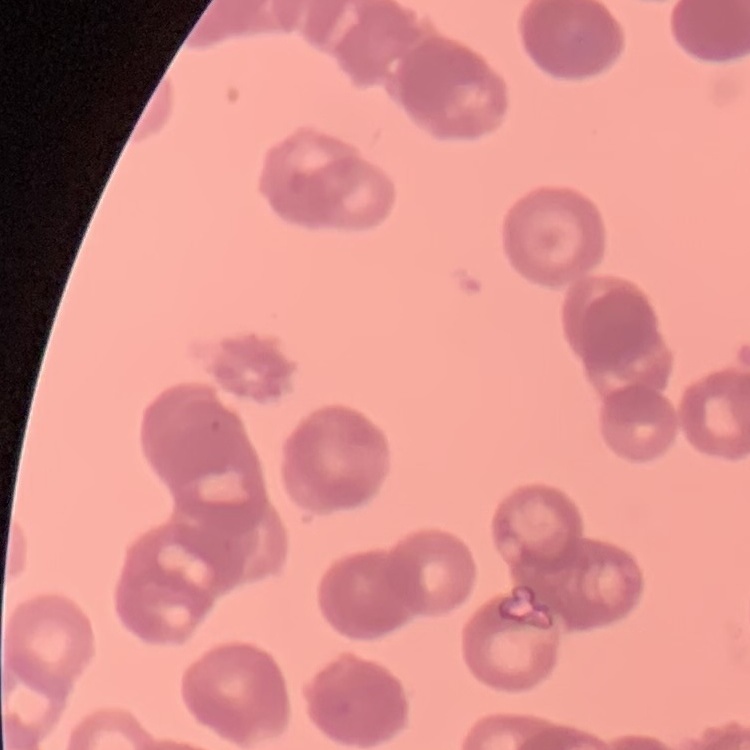

Summary:
  - Red blood cell morphology: rouleaux formation
  - Preparation: thin blood smear
  - Image type: square crop of a larger photomicrograph
  - Stain: Field's or Giemsa